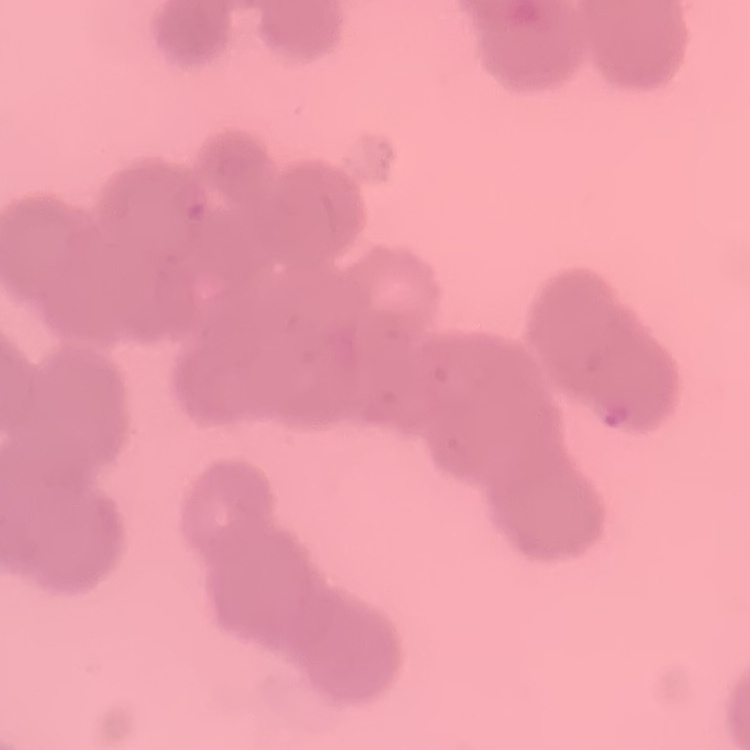

red_blood_cell_morphology: rouleaux formation
stain: Field's or Giemsa
preparation: thin blood smear
image_type: square crop of a larger photomicrograph